Report the malaria status of this cell.
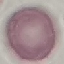
Uninfected.

Summary:
  - Image type: automatically extracted cell patch, resized to 64 × 64 pixels
  - Preparation: thin smear
  - Stain: Giemsa
  - Capture: smartphone through the microscope eyepiece